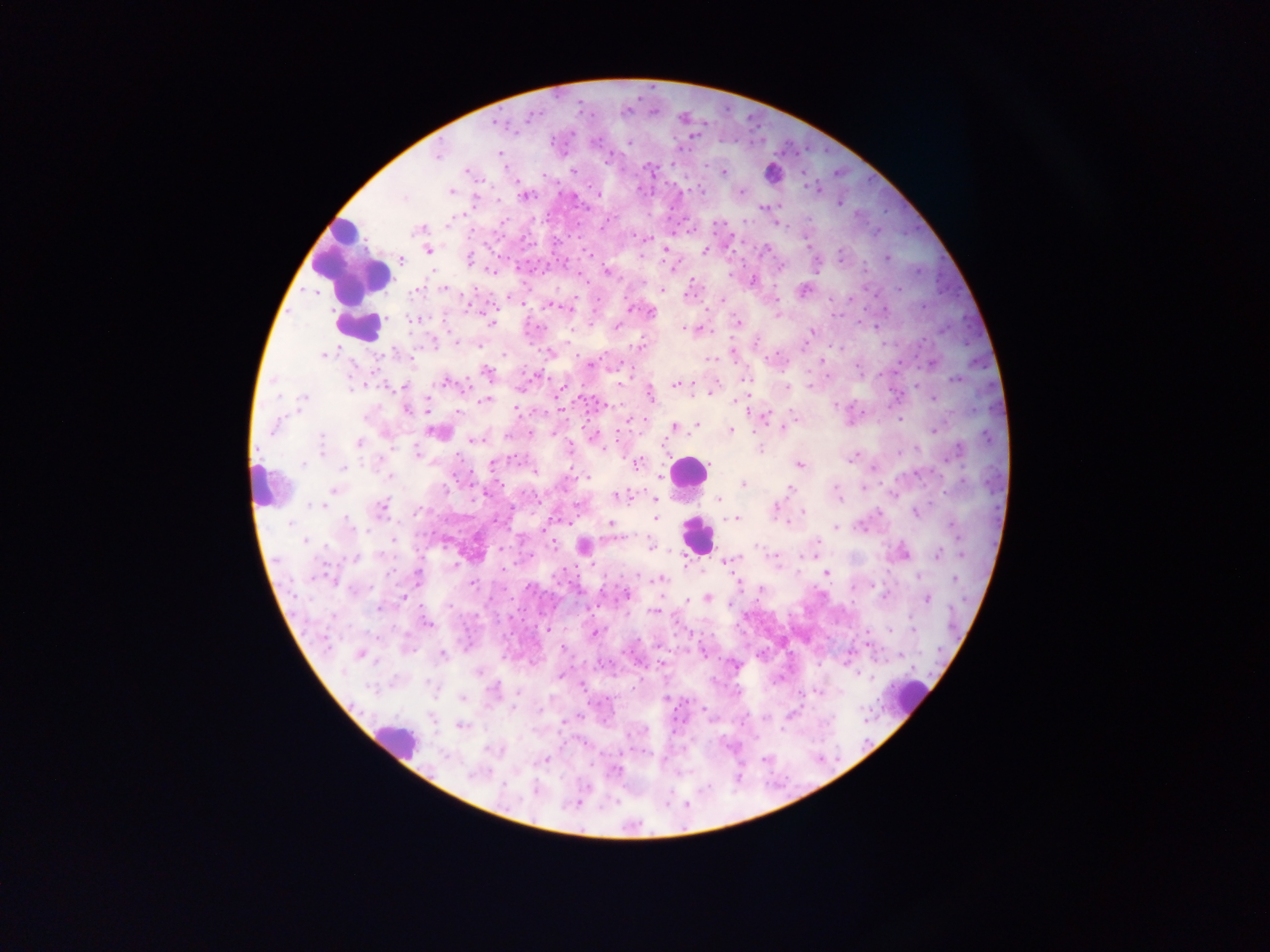
Approximate centers as x y in pixels.
Summary:
  - Leukocyte locations: 354 258; 360 324; 690 470; 261 484; 696 539; 915 693; 397 744
  - Malaria parasite locations: 530 116; 493 124; 501 128; 573 131; 695 136; 691 140; 595 144; 629 144; 438 155; 607 158; 643 163; 575 171; 724 172; 837 174; 638 185; 808 185; 816 187; 449 193; 576 193; 525 196; 403 198; 838 200; 778 205; 769 208; 763 210; 603 224; 645 239; 806 242; 663 248; 765 248; 428 250; 701 250; 705 250; 590 255; 886 258; 492 272; 607 274; 660 289; 897 290; 722 301; 555 305; 471 307; 628 309; 885 309; 652 312; 413 320; 735 321; 490 322; 617 326; 874 327; 685 328; 688 330; 811 331; 757 341; 457 344; 434 345; 479 346; 338 349; 327 353; 321 355; 932 360; 587 361; 711 361; 356 366; 352 371; 487 371; 538 372; 744 378; 955 379; 448 382; 465 383; 404 385; 674 386; 788 387; 561 390; 712 391; 709 394; 304 397; 278 399; 651 399; 932 401; 484 402; 732 402; 737 402; 604 405; 425 407; 407 408; 518 412; 794 412; 765 414; 632 420; 899 420; 697 425; 274 427; 673 427; 783 427; 431 430; 730 431; 933 431; 321 433; 529 433; 595 435; 321 437; 474 440; 360 443; 604 445; 322 449; 607 449; 760 450; 959 450; 416 451; 512 456; 851 458; 302 464; 637 465; 799 465; 493 466; 343 467; 873 471; 391 477; 588 477; 743 484; 334 491; 790 492; 483 494; 629 494; 616 495; 893 497; 653 499; 718 499; 839 499; 313 504; 776 505; 322 506; 381 508; 419 512; 804 512; 916 512; 658 514; 735 518; 787 522; 348 523; 610 524; 289 526; 836 528; 956 530; 613 537; 393 538; 817 541; 306 542; 757 543; 651 544; 553 545; 501 551; 379 553; 937 554; 354 558; 736 559; 728 560; 776 562; 454 566; 392 572; 642 574; 826 574; 316 576; 416 577; 918 577; 661 579; 955 580; 738 583; 473 584; 348 588; 759 591; 626 595; 707 598; 404 599; 926 599; 687 601; 379 608; 656 610; 332 616; 910 618; 428 624; 549 629; 600 630; 890 631; 595 632; 358 654; 440 655; 478 672; 559 675; 582 685; 519 692; 518 695; 817 695; 666 698; 513 710; 705 714; 795 714; 572 720; 784 728; 765 760; 618 768; 471 775; 502 788
  - Preparation: thick blood film
  - Capture: mobile-phone photograph through a microscope
  - Image size: 1270×952 pixels
  - Country: Ghana
  - Field of view: single